State which cell type is depicted.
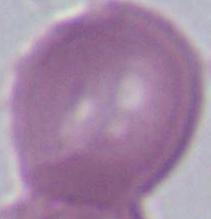

An erythrocyte.

Micrograph. Captured at 1000x magnification.